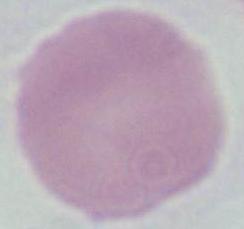

An erythrocyte is seen. Captured at 1000x magnification. Photomicrograph.